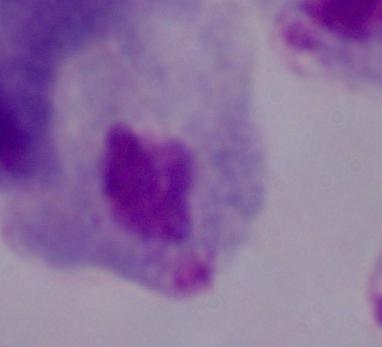
Summary:
  - Identification: trichomonad
  - Magnification: 1000x
  - Modality: photomicrograph